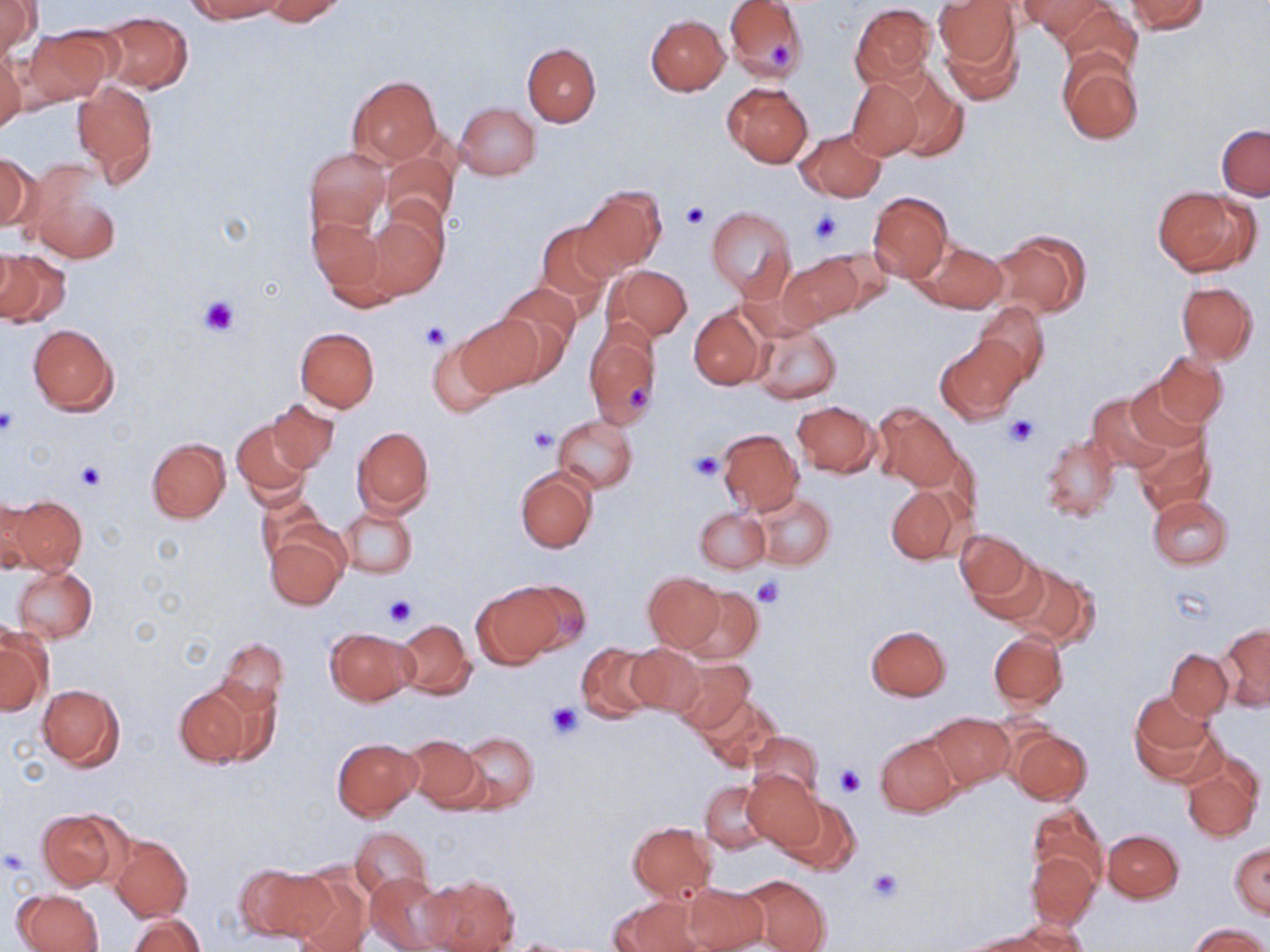
Approximate bounding boxes as (x1, y1, x2, y2) in pixels. Platelet locations: (765, 39, 793, 68), (679, 202, 710, 231), (808, 207, 845, 247), (198, 292, 240, 336), (421, 321, 450, 349), (624, 384, 650, 409), (0, 409, 19, 435), (1004, 415, 1038, 447), (527, 426, 556, 453), (691, 453, 725, 480), (77, 461, 105, 492), (751, 575, 785, 608), (381, 595, 416, 630), (546, 701, 584, 738), (837, 765, 867, 797), (2, 848, 29, 874), (865, 868, 904, 902). Uninfected red blood cell locations: (185, 0, 285, 22), (262, 0, 350, 24), (724, 0, 808, 81), (934, 0, 1019, 76), (1021, 0, 1116, 45), (1126, 0, 1209, 34), (1, 2, 39, 60), (1055, 2, 1142, 78), (850, 3, 937, 88), (95, 12, 193, 92), (645, 14, 729, 95), (20, 27, 115, 108), (522, 43, 599, 127), (0, 49, 25, 136), (1058, 55, 1144, 144), (881, 67, 969, 163), (347, 76, 442, 167), (845, 77, 923, 160), (72, 80, 159, 186), (722, 81, 813, 167), (455, 102, 540, 181), (1216, 124, 1269, 200), (795, 128, 885, 201), (305, 148, 391, 235), (381, 149, 459, 230), (0, 153, 37, 234), (25, 162, 122, 265), (577, 186, 665, 275), (1153, 186, 1256, 276), (867, 191, 953, 283), (364, 206, 448, 300), (705, 206, 797, 301), (306, 215, 390, 299), (536, 220, 616, 313), (990, 229, 1091, 318), (917, 241, 1007, 314), (806, 246, 892, 318), (0, 248, 71, 328), (777, 255, 861, 329), (605, 264, 692, 343), (1176, 280, 1258, 366), (496, 281, 580, 370), (973, 301, 1050, 383), (689, 306, 768, 389), (458, 313, 545, 396), (748, 315, 841, 405), (584, 319, 662, 431), (28, 324, 118, 415), (295, 327, 379, 412), (934, 334, 1028, 425), (428, 336, 503, 418), (1147, 352, 1228, 431), (1123, 376, 1211, 453), (1087, 392, 1176, 471), (267, 400, 340, 473), (791, 401, 880, 477), (873, 403, 961, 491), (553, 415, 638, 493), (232, 418, 314, 505), (352, 426, 434, 517), (716, 428, 805, 516), (1131, 429, 1214, 517), (1041, 434, 1120, 522), (146, 438, 230, 523), (516, 467, 596, 552), (885, 485, 966, 564), (255, 488, 328, 564), (750, 492, 834, 569), (1, 495, 43, 574), (5, 495, 87, 573), (1147, 495, 1233, 570), (339, 504, 418, 579), (695, 507, 769, 573), (266, 530, 348, 610), (955, 530, 1033, 604), (967, 553, 1050, 625), (1007, 562, 1099, 649), (11, 566, 97, 643), (643, 572, 725, 651), (472, 580, 571, 666), (681, 586, 762, 665), (393, 618, 475, 700), (1219, 623, 1270, 710), (867, 625, 951, 700), (326, 628, 418, 705), (1, 629, 50, 715), (989, 632, 1069, 711), (215, 637, 287, 715), (576, 642, 660, 722), (626, 643, 703, 716), (1166, 649, 1234, 720), (669, 657, 753, 734), (173, 683, 264, 769), (37, 684, 124, 769), (1129, 692, 1220, 783), (696, 694, 783, 772), (929, 712, 1014, 789), (1009, 727, 1092, 804), (750, 731, 823, 800), (458, 732, 538, 813), (876, 733, 959, 817), (403, 734, 485, 810), (333, 738, 423, 821), (1183, 755, 1261, 843), (741, 770, 825, 852), (701, 780, 773, 854), (779, 796, 860, 874), (1027, 802, 1106, 888), (37, 809, 125, 890), (627, 822, 716, 902), (351, 826, 431, 899), (1103, 829, 1184, 902), (109, 835, 192, 922), (1230, 844, 1270, 918), (1026, 849, 1099, 927), (235, 863, 330, 942), (287, 868, 373, 952), (366, 871, 453, 952), (738, 873, 833, 952), (420, 876, 520, 952), (681, 880, 769, 952), (14, 889, 105, 952), (610, 897, 702, 952), (128, 914, 205, 952), (1003, 920, 1094, 950), (1189, 924, 1268, 952), (961, 932, 1055, 951). Slide-level diagnosis: no evidence of blood parasites. Thin blood film. Optical microscopy. Single field of view. 1000x magnification. May-Grünwald-Giemsa stain. Image is 1270×952 pixels.